Locate and identify every blood parasite.
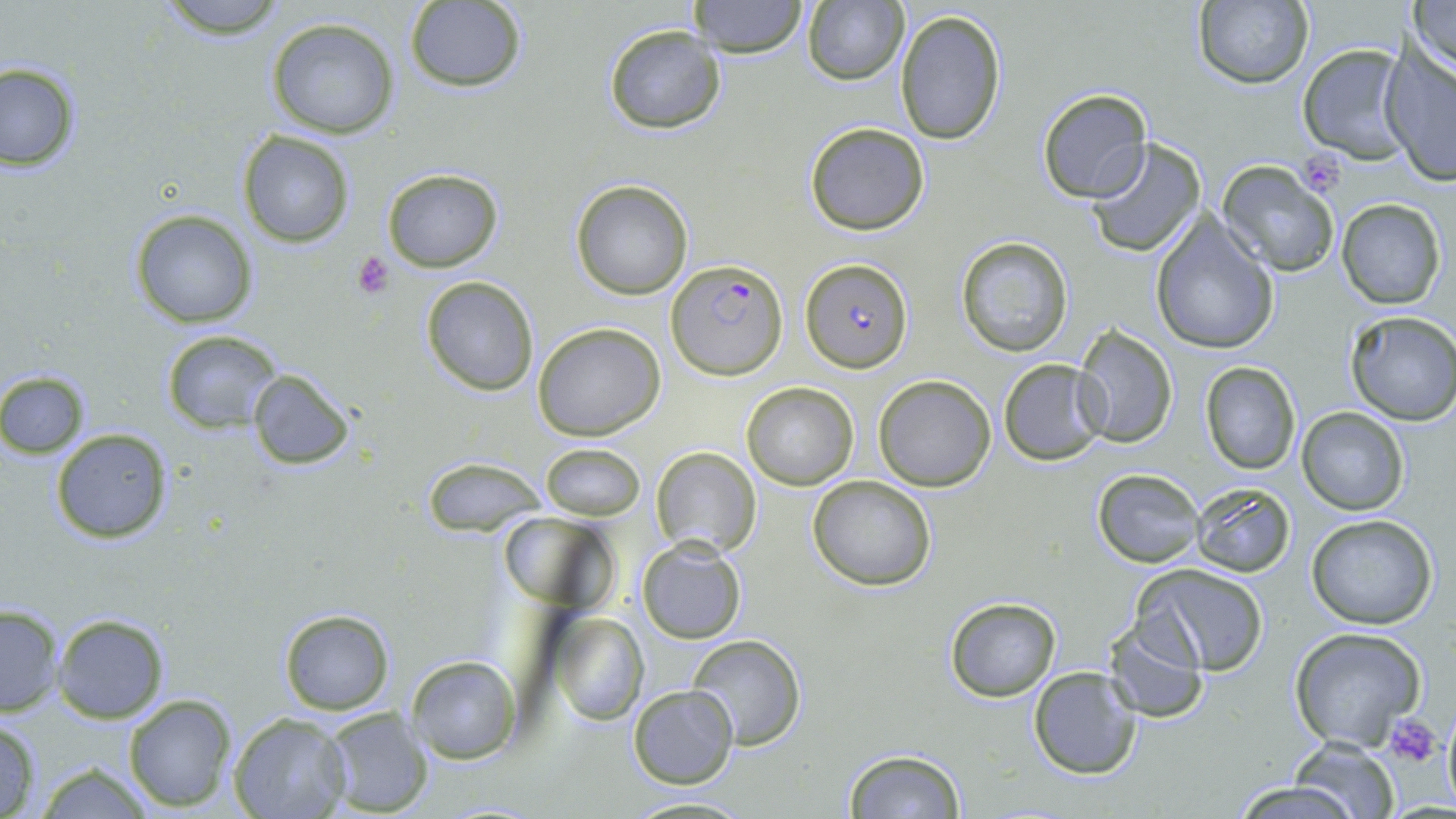

Approximate bounding boxes as [x1, y1, x2, y2] in pixels.
Plasmodium falciparum-infected red blood cells: [666, 257, 788, 382], [801, 259, 911, 372].
No Plasmodium ovale, Plasmodium malariae, Plasmodium vivax, Babesia divergens, or Trypanosoma brucei observed.

Summary:
  - Platelet locations: [1298, 153, 1348, 194], [351, 252, 393, 299], [1389, 714, 1444, 767]
  - Uninfected red blood cell locations: [153, 0, 291, 38], [687, 0, 809, 57], [1408, 0, 1456, 79], [1190, 1, 1315, 89], [402, 2, 528, 91], [801, 2, 909, 85], [895, 7, 1008, 146], [264, 16, 402, 140], [602, 25, 728, 134], [1294, 44, 1415, 163], [1377, 50, 1455, 183], [0, 63, 82, 171], [1035, 88, 1154, 205], [804, 121, 930, 236], [236, 129, 355, 248], [1084, 139, 1208, 259], [1217, 162, 1340, 277], [382, 168, 503, 272], [569, 177, 694, 300], [1334, 198, 1446, 309], [128, 208, 259, 329], [1149, 215, 1281, 356], [954, 236, 1072, 356], [420, 275, 541, 395], [1343, 312, 1456, 426], [534, 322, 666, 441], [1073, 326, 1178, 447], [162, 329, 283, 434], [997, 358, 1109, 465], [1197, 360, 1302, 475], [246, 366, 359, 472], [0, 370, 89, 458], [874, 374, 996, 491], [741, 383, 858, 490], [1296, 406, 1409, 515], [50, 426, 174, 543], [538, 442, 646, 520], [649, 447, 761, 558], [424, 460, 543, 535], [1092, 469, 1204, 567], [807, 475, 937, 591], [1190, 483, 1295, 578], [1304, 512, 1438, 630], [500, 514, 616, 612], [635, 537, 749, 645], [1134, 564, 1269, 676], [943, 597, 1062, 702], [0, 604, 64, 718], [279, 608, 394, 715], [547, 610, 647, 725], [52, 611, 170, 723], [1103, 616, 1210, 723], [1287, 629, 1428, 753], [686, 636, 810, 750], [406, 654, 522, 765], [1028, 666, 1145, 781], [627, 683, 739, 788], [122, 693, 237, 812], [318, 708, 435, 817], [227, 713, 350, 819], [0, 719, 42, 817], [1285, 738, 1400, 817], [843, 747, 967, 817], [31, 762, 157, 819], [1230, 780, 1362, 819], [619, 795, 758, 817]
  - Slide-level diagnosis: Plasmodium falciparum
  - Field of view: single
  - Modality: light microscopy
  - Stain: May-Grünwald-Giemsa
  - Preparation: thin blood film
  - Image size: 1456×819 pixels
  - Magnification: 1000x